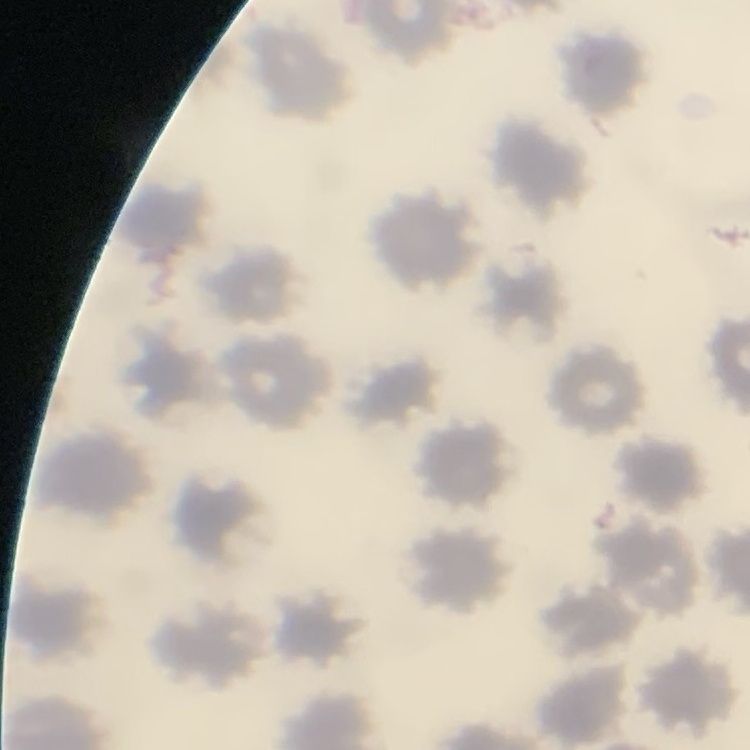

erythrocyte_morphology: no rouleaux formation
preparation: thin blood film
stain: Field's or Giemsa
image_type: square crop of a larger photomicrograph